Report the malaria status of this cell.
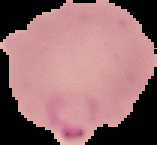

It is parasitized.

image size = 157×145 pixels
preparation = thin blood smear
image type = segmented cell region with the area outside set to black